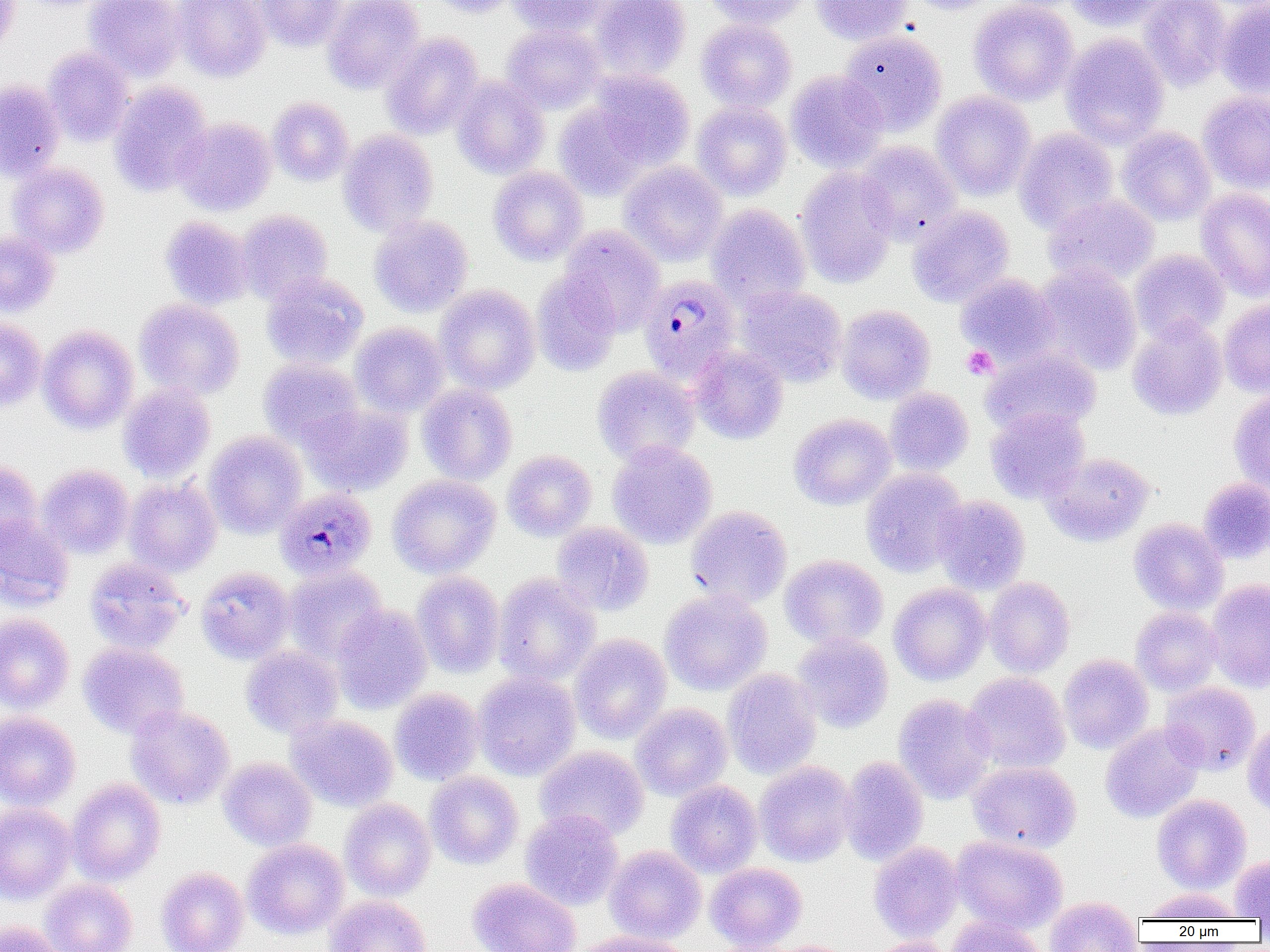

Approximate bounding boxes as named x1/y1/x2/y2 corners in pixels. Uninfected red blood cell locations: (x1=0, y1=0, x2=19, y2=54), (x1=84, y1=0, x2=185, y2=81), (x1=173, y1=0, x2=271, y2=82), (x1=254, y1=0, x2=347, y2=51), (x1=322, y1=0, x2=425, y2=94), (x1=426, y1=0, x2=520, y2=17), (x1=507, y1=0, x2=612, y2=36), (x1=589, y1=0, x2=691, y2=81), (x1=705, y1=0, x2=813, y2=29), (x1=811, y1=0, x2=913, y2=45), (x1=907, y1=0, x2=1001, y2=15), (x1=968, y1=0, x2=1079, y2=106), (x1=1065, y1=0, x2=1169, y2=30), (x1=1138, y1=0, x2=1231, y2=91), (x1=1217, y1=0, x2=1270, y2=99), (x1=696, y1=19, x2=797, y2=111), (x1=501, y1=24, x2=606, y2=114), (x1=839, y1=30, x2=947, y2=135), (x1=382, y1=33, x2=483, y2=139), (x1=1060, y1=33, x2=1169, y2=149), (x1=44, y1=47, x2=134, y2=146), (x1=588, y1=70, x2=695, y2=170), (x1=786, y1=71, x2=889, y2=172), (x1=451, y1=76, x2=549, y2=179), (x1=0, y1=80, x2=65, y2=181), (x1=109, y1=82, x2=212, y2=196), (x1=931, y1=91, x2=1035, y2=200), (x1=1198, y1=91, x2=1270, y2=194), (x1=268, y1=97, x2=354, y2=186), (x1=692, y1=101, x2=792, y2=200), (x1=554, y1=102, x2=652, y2=200), (x1=172, y1=117, x2=277, y2=216), (x1=1117, y1=126, x2=1216, y2=225), (x1=1014, y1=128, x2=1118, y2=233), (x1=338, y1=129, x2=438, y2=237), (x1=855, y1=141, x2=961, y2=244), (x1=619, y1=161, x2=727, y2=266), (x1=8, y1=162, x2=109, y2=258), (x1=488, y1=166, x2=588, y2=265), (x1=794, y1=166, x2=898, y2=288), (x1=1195, y1=188, x2=1270, y2=301), (x1=1043, y1=194, x2=1160, y2=287), (x1=706, y1=204, x2=811, y2=309), (x1=907, y1=205, x2=1014, y2=307), (x1=236, y1=210, x2=333, y2=304), (x1=369, y1=215, x2=473, y2=317), (x1=159, y1=216, x2=253, y2=310), (x1=559, y1=225, x2=666, y2=334), (x1=0, y1=230, x2=59, y2=317), (x1=1130, y1=249, x2=1230, y2=343), (x1=1035, y1=263, x2=1142, y2=375), (x1=531, y1=269, x2=622, y2=376), (x1=263, y1=273, x2=368, y2=369), (x1=956, y1=273, x2=1060, y2=366), (x1=435, y1=285, x2=540, y2=394), (x1=737, y1=286, x2=848, y2=386), (x1=1219, y1=298, x2=1270, y2=397), (x1=135, y1=299, x2=244, y2=399), (x1=836, y1=304, x2=935, y2=404), (x1=1127, y1=315, x2=1228, y2=420), (x1=0, y1=318, x2=46, y2=411), (x1=350, y1=323, x2=449, y2=416), (x1=38, y1=325, x2=139, y2=433), (x1=688, y1=345, x2=789, y2=445), (x1=981, y1=347, x2=1101, y2=437), (x1=259, y1=358, x2=364, y2=449), (x1=592, y1=366, x2=700, y2=466), (x1=117, y1=382, x2=216, y2=483), (x1=417, y1=383, x2=518, y2=485), (x1=885, y1=387, x2=974, y2=476), (x1=1228, y1=390, x2=1270, y2=495), (x1=301, y1=403, x2=413, y2=496), (x1=986, y1=407, x2=1090, y2=503), (x1=789, y1=413, x2=896, y2=510), (x1=204, y1=431, x2=307, y2=538), (x1=607, y1=440, x2=717, y2=549), (x1=502, y1=450, x2=597, y2=541), (x1=1041, y1=452, x2=1155, y2=546), (x1=0, y1=460, x2=43, y2=553), (x1=37, y1=465, x2=134, y2=559), (x1=861, y1=467, x2=968, y2=577), (x1=387, y1=475, x2=500, y2=578), (x1=124, y1=478, x2=222, y2=576), (x1=1198, y1=478, x2=1270, y2=564), (x1=933, y1=495, x2=1030, y2=594), (x1=686, y1=505, x2=792, y2=608), (x1=0, y1=515, x2=74, y2=610), (x1=1128, y1=518, x2=1229, y2=615), (x1=552, y1=521, x2=654, y2=616), (x1=780, y1=554, x2=888, y2=649), (x1=83, y1=557, x2=189, y2=654), (x1=283, y1=565, x2=388, y2=664), (x1=196, y1=566, x2=295, y2=664), (x1=412, y1=571, x2=506, y2=678), (x1=493, y1=573, x2=601, y2=686), (x1=985, y1=576, x2=1076, y2=678), (x1=1206, y1=579, x2=1270, y2=693), (x1=888, y1=583, x2=992, y2=685), (x1=660, y1=589, x2=772, y2=695), (x1=331, y1=604, x2=433, y2=714), (x1=1130, y1=606, x2=1223, y2=696), (x1=0, y1=614, x2=75, y2=713), (x1=792, y1=633, x2=893, y2=733), (x1=569, y1=634, x2=672, y2=744), (x1=78, y1=642, x2=189, y2=739), (x1=241, y1=645, x2=343, y2=738), (x1=1058, y1=654, x2=1153, y2=754), (x1=722, y1=668, x2=822, y2=780), (x1=473, y1=670, x2=580, y2=781), (x1=963, y1=672, x2=1071, y2=774), (x1=1159, y1=682, x2=1260, y2=775), (x1=390, y1=688, x2=484, y2=784), (x1=893, y1=694, x2=996, y2=804), (x1=630, y1=703, x2=733, y2=800), (x1=126, y1=705, x2=234, y2=809), (x1=0, y1=711, x2=81, y2=810), (x1=287, y1=714, x2=398, y2=811), (x1=1243, y1=721, x2=1270, y2=815), (x1=1100, y1=722, x2=1205, y2=823), (x1=535, y1=745, x2=649, y2=841), (x1=838, y1=756, x2=929, y2=866), (x1=218, y1=757, x2=317, y2=851), (x1=754, y1=760, x2=856, y2=867), (x1=967, y1=760, x2=1082, y2=852), (x1=425, y1=771, x2=523, y2=870), (x1=67, y1=779, x2=166, y2=885), (x1=666, y1=780, x2=762, y2=877), (x1=1152, y1=794, x2=1251, y2=893), (x1=339, y1=798, x2=436, y2=902), (x1=0, y1=802, x2=76, y2=904), (x1=520, y1=809, x2=623, y2=910), (x1=951, y1=835, x2=1068, y2=933), (x1=243, y1=838, x2=348, y2=939), (x1=868, y1=841, x2=963, y2=943), (x1=605, y1=845, x2=706, y2=943), (x1=1230, y1=854, x2=1270, y2=920), (x1=705, y1=862, x2=807, y2=951), (x1=156, y1=866, x2=249, y2=952), (x1=467, y1=877, x2=581, y2=952), (x1=39, y1=878, x2=137, y2=952), (x1=1141, y1=888, x2=1243, y2=922), (x1=323, y1=895, x2=432, y2=952), (x1=1044, y1=896, x2=1143, y2=952), (x1=946, y1=915, x2=1047, y2=952), (x1=0, y1=920, x2=68, y2=952), (x1=568, y1=931, x2=695, y2=952), (x1=863, y1=937, x2=956, y2=952). Platelet locations: (x1=961, y1=346, x2=997, y2=380). Plasmodium malariae-infected red blood cell locations: (x1=639, y1=275, x2=741, y2=382), (x1=275, y1=491, x2=377, y2=574). Slide-level diagnosis: Plasmodium malariae. Thin blood smear. Light microscopy. One field of a larger specimen. Captured at 1000x magnification. Image is 1270×952 pixels.